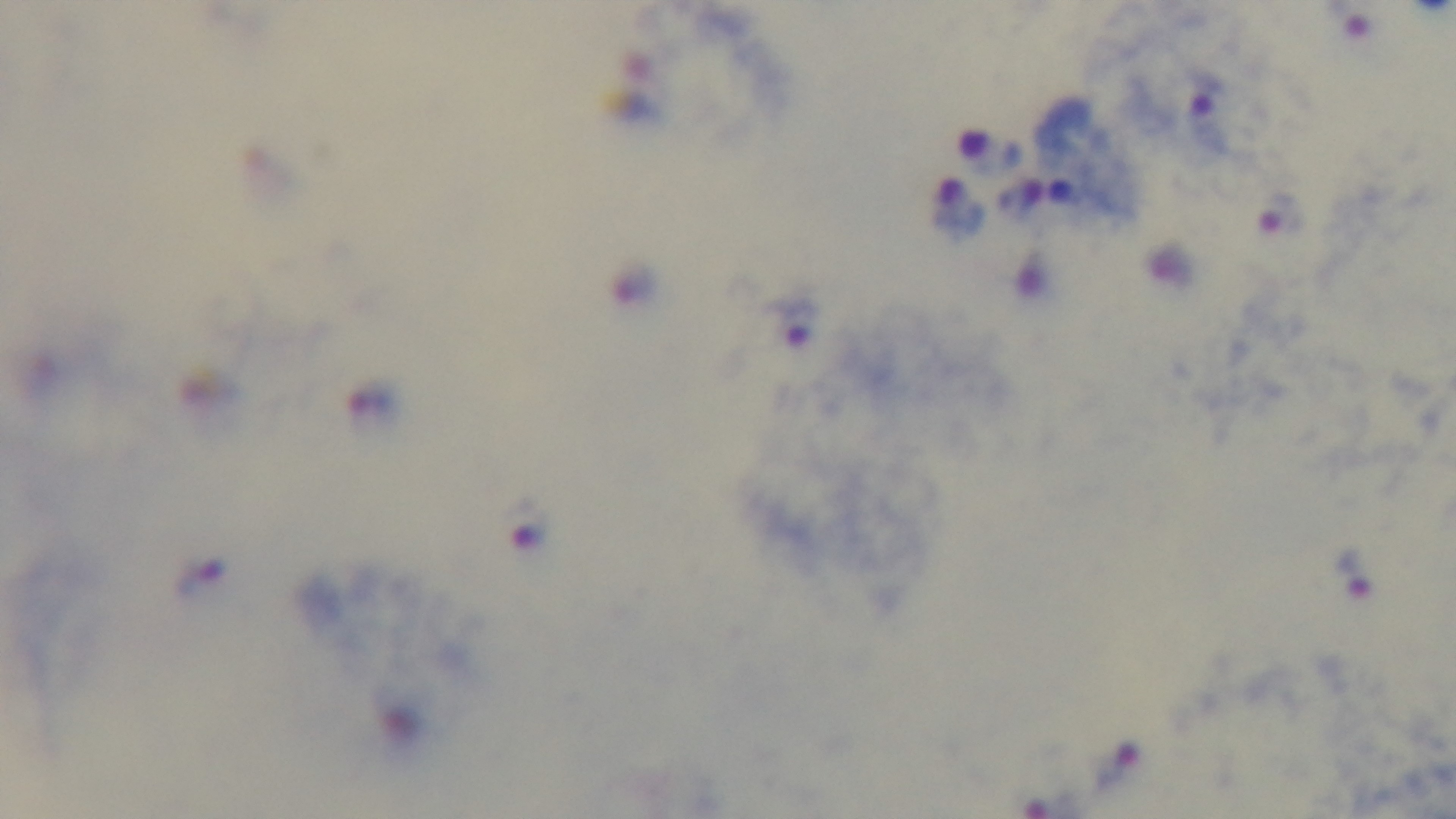 100x oil-immersion objective. Giemsa-stained. One field from the slide. Malaria status: infected. Preparation: thick smear. Photomicrograph. Mounted 4K digital camera.